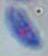
Summary:
  - Magnification: 1000x
  - Identification: Toxoplasma gondii
  - Modality: micrograph